Classify this cell by malaria status.
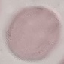

Uninfected.

{
  "stain": "Giemsa",
  "capture": "smartphone camera at the microscope eyepiece",
  "image_type": "cell patch, automatically extracted from a larger field of view and resized to 64 × 64 pixels",
  "preparation": "thin smear"
}